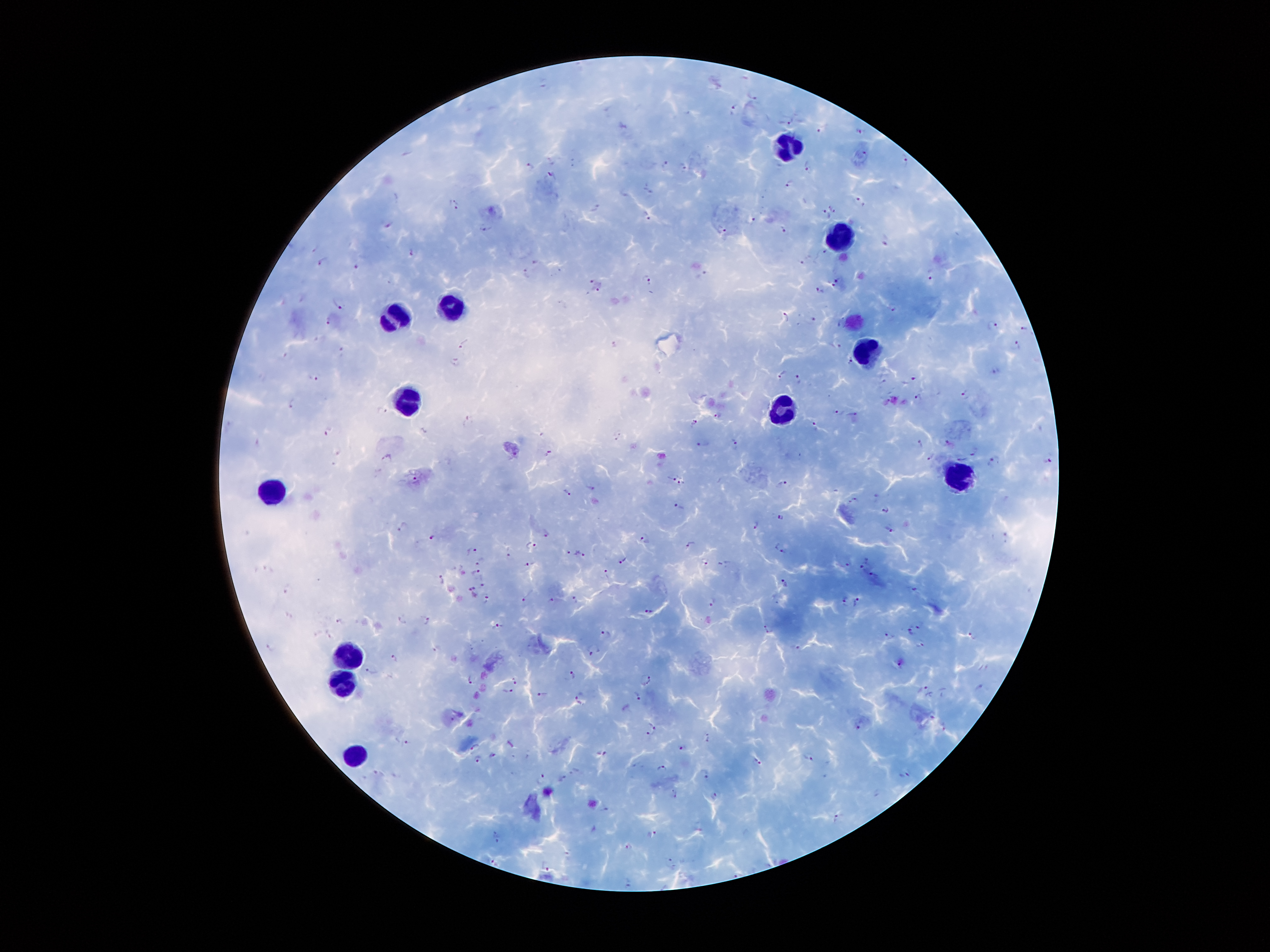

Approximate object centers, in pixels from the top-left corner. Plasmodium parasite locations: (x=752, y=98), (x=734, y=108), (x=789, y=122), (x=623, y=126), (x=821, y=130), (x=859, y=131), (x=864, y=154), (x=905, y=160), (x=665, y=165), (x=808, y=165), (x=528, y=166), (x=684, y=167), (x=551, y=175), (x=790, y=184), (x=649, y=190), (x=456, y=202), (x=859, y=202), (x=454, y=207), (x=594, y=207), (x=832, y=207), (x=648, y=215), (x=825, y=215), (x=752, y=219), (x=388, y=221), (x=721, y=228), (x=485, y=229), (x=781, y=229), (x=885, y=240), (x=411, y=252), (x=824, y=252), (x=800, y=260), (x=322, y=261), (x=537, y=262), (x=357, y=266), (x=526, y=273), (x=702, y=273), (x=930, y=274), (x=650, y=278), (x=840, y=280), (x=590, y=281), (x=597, y=289), (x=818, y=292), (x=339, y=302), (x=892, y=306), (x=785, y=316), (x=813, y=318), (x=329, y=320), (x=992, y=324), (x=1023, y=327), (x=1017, y=343), (x=463, y=344), (x=839, y=344), (x=614, y=345), (x=342, y=352), (x=284, y=354), (x=850, y=360), (x=455, y=361), (x=996, y=370), (x=782, y=373), (x=313, y=375), (x=914, y=377), (x=799, y=379), (x=965, y=393), (x=919, y=397), (x=291, y=401), (x=381, y=410), (x=838, y=410), (x=717, y=412), (x=854, y=414), (x=469, y=420), (x=694, y=423), (x=816, y=426), (x=329, y=432), (x=619, y=435), (x=736, y=439), (x=703, y=443), (x=921, y=443), (x=948, y=443), (x=974, y=450), (x=550, y=452), (x=930, y=456), (x=387, y=457), (x=964, y=458), (x=993, y=460), (x=1048, y=460), (x=672, y=476), (x=416, y=479), (x=681, y=480), (x=783, y=484), (x=591, y=487), (x=568, y=493), (x=877, y=497), (x=851, y=499), (x=680, y=506), (x=886, y=508), (x=781, y=516), (x=756, y=524), (x=402, y=528), (x=890, y=529), (x=547, y=534), (x=432, y=537), (x=1006, y=537), (x=645, y=539), (x=690, y=543), (x=529, y=546), (x=782, y=546), (x=568, y=551), (x=471, y=552), (x=509, y=552), (x=582, y=554), (x=623, y=560), (x=479, y=561), (x=703, y=563), (x=529, y=564), (x=725, y=564), (x=864, y=564), (x=846, y=565), (x=476, y=572), (x=607, y=573), (x=873, y=574), (x=442, y=578), (x=785, y=582), (x=482, y=585), (x=289, y=588), (x=913, y=589), (x=473, y=590), (x=487, y=598), (x=525, y=598), (x=575, y=598), (x=550, y=600), (x=843, y=600), (x=712, y=601), (x=856, y=601), (x=649, y=612), (x=401, y=618), (x=429, y=620), (x=341, y=621), (x=497, y=625), (x=918, y=625), (x=768, y=627), (x=910, y=630), (x=607, y=632), (x=330, y=633), (x=973, y=633), (x=889, y=636), (x=921, y=644), (x=271, y=645), (x=436, y=648), (x=795, y=648), (x=594, y=652), (x=394, y=658), (x=900, y=663), (x=371, y=670), (x=574, y=674), (x=648, y=677), (x=471, y=679), (x=515, y=682), (x=981, y=687), (x=922, y=689), (x=509, y=691), (x=638, y=692), (x=541, y=693), (x=579, y=697), (x=860, y=724), (x=654, y=727), (x=945, y=727), (x=648, y=734), (x=708, y=738), (x=405, y=741), (x=473, y=745), (x=683, y=749), (x=603, y=752), (x=493, y=756), (x=808, y=757), (x=477, y=759), (x=758, y=762), (x=661, y=767), (x=707, y=774), (x=906, y=774), (x=542, y=778), (x=676, y=792), (x=716, y=795), (x=604, y=807), (x=835, y=815), (x=497, y=835), (x=652, y=835), (x=628, y=846), (x=567, y=851), (x=493, y=860), (x=672, y=860), (x=546, y=865), (x=630, y=882). Leukocyte locations: (x=787, y=143), (x=843, y=231), (x=452, y=304), (x=395, y=315), (x=875, y=348), (x=406, y=392), (x=780, y=409), (x=959, y=477), (x=272, y=487), (x=346, y=651), (x=342, y=682), (x=357, y=752). Patient malaria status: positive for Plasmodium falciparum. Single field of view. 100x magnification. Giemsa stain. Image is 1270×952 pixels. Smartphone photograph taken through the microscope eyepiece. Thick blood smear.